Assess this cell for malaria.
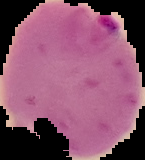

It is parasitized.

{
  "preparation": "thin blood film",
  "image_type": "segmented cell region with the area outside set to black",
  "image_size": "145×160 pixels"
}